Give the position of every Plasmodium parasite visible.
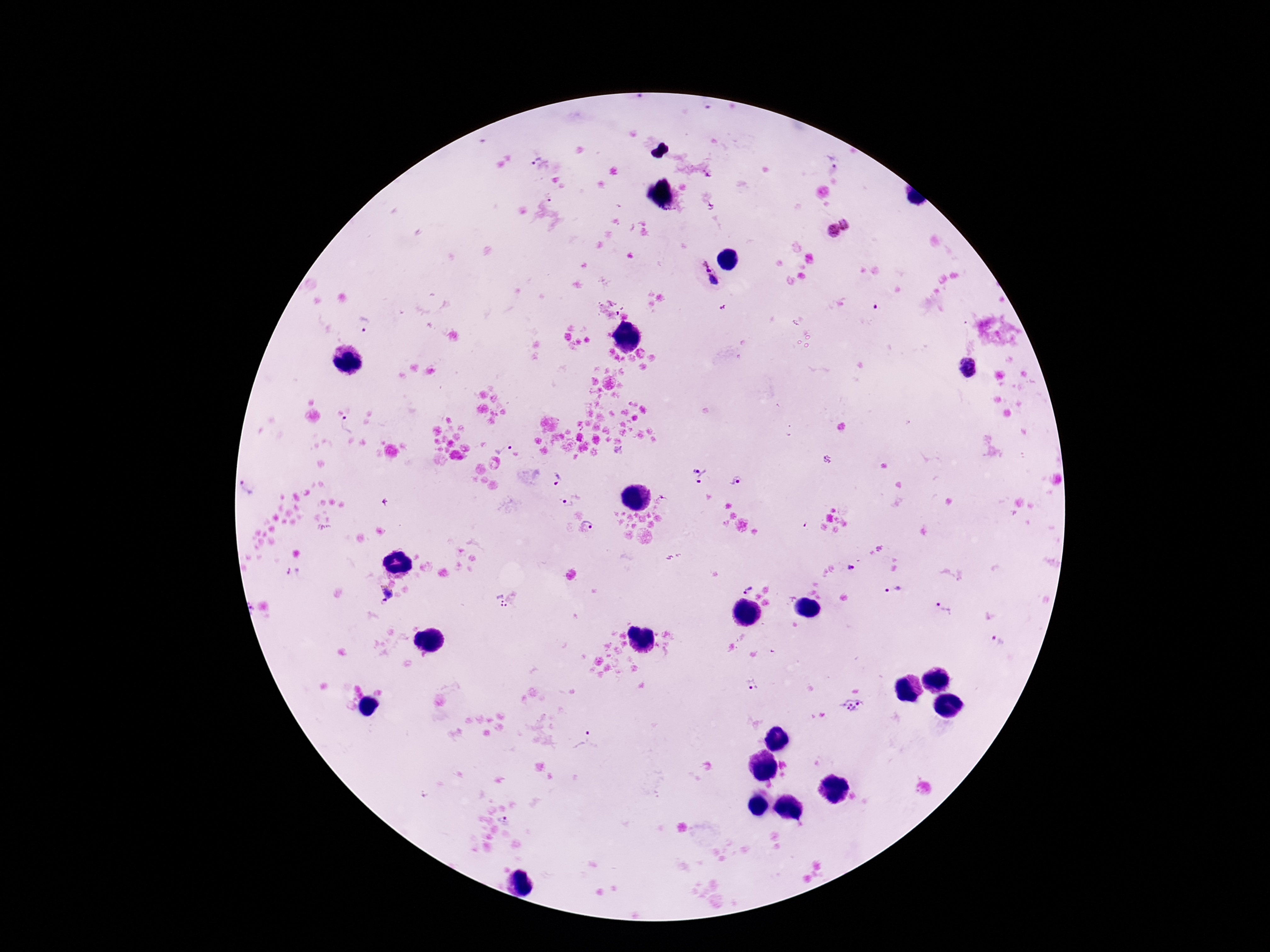

Approximate centers as {x, y} in pixels.
Plasmodium parasites: {534, 157}, {551, 197}, {849, 221}, {833, 230}, {706, 264}, {713, 280}, {876, 307}, {365, 326}, {968, 369}, {347, 424}, {503, 447}, {699, 475}, {557, 479}, {736, 480}, {249, 486}, {571, 501}, {662, 502}, {592, 521}, {851, 567}, {295, 574}, {747, 589}, {894, 590}, {388, 592}, {504, 599}, {384, 600}, {946, 609}, {996, 639}, {753, 685}, {851, 706}, {586, 745}, {505, 818}.

Summary:
  - Image size: 1270×952 pixels
  - Preparation: thick blood smear
  - Magnification: 100x
  - Patient malaria status: positive
  - Stain: Giemsa
  - Capture: smartphone camera through the microscope eyepiece
  - Field of view: single